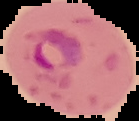
image type = segmented cell region on a black background
image size = 139×121 pixels
malaria status = parasitized
preparation = thin blood smear